Report the malaria status.
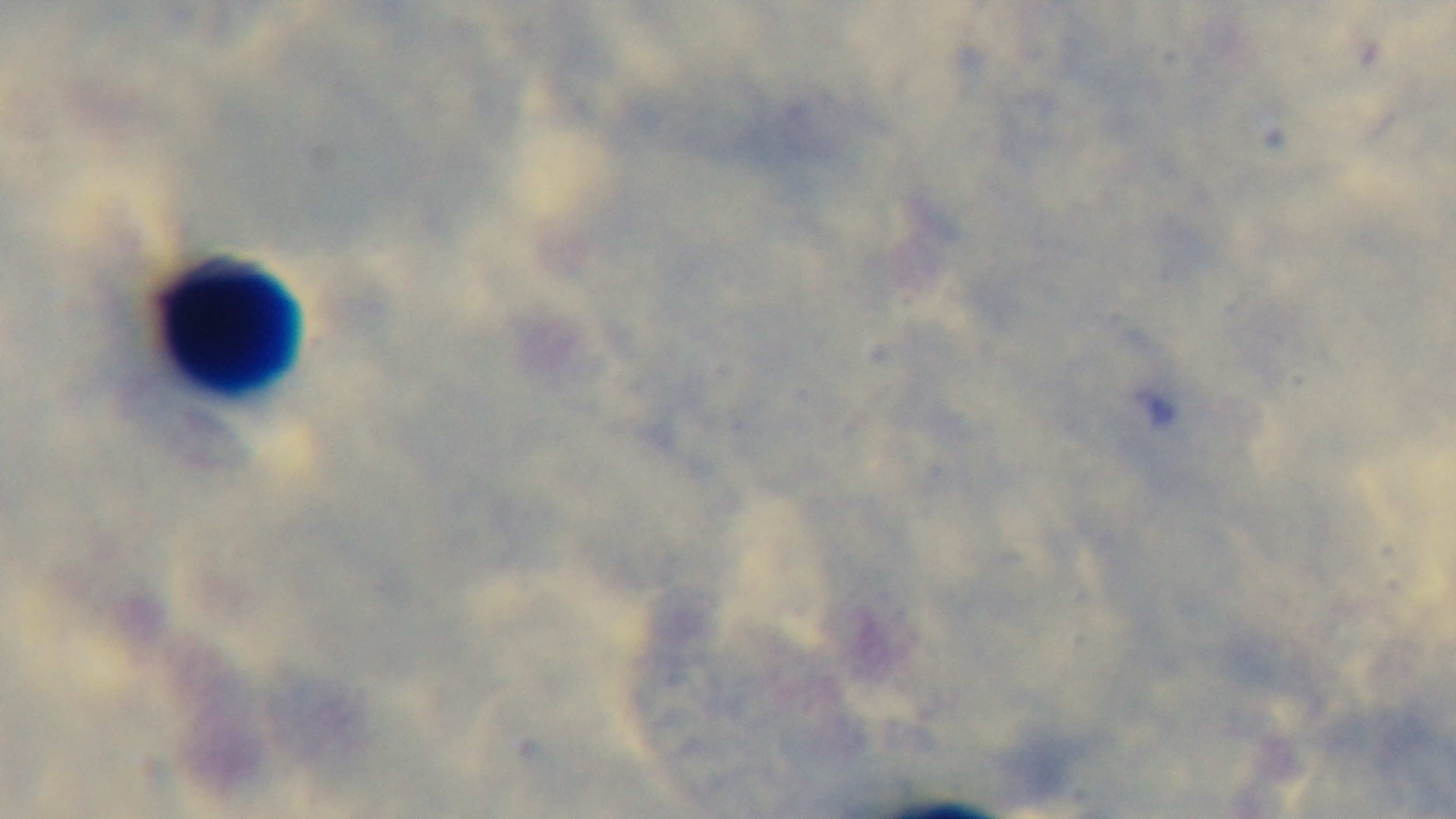

It is uninfected.

Summary:
  - Field of view: one from the slide
  - Objective: 100x oil immersion
  - Capture: mounted 4K digital camera
  - Modality: light microscopy
  - Preparation: thick blood film
  - Stain: Giemsa